Locate every blood parasite and identify its species.
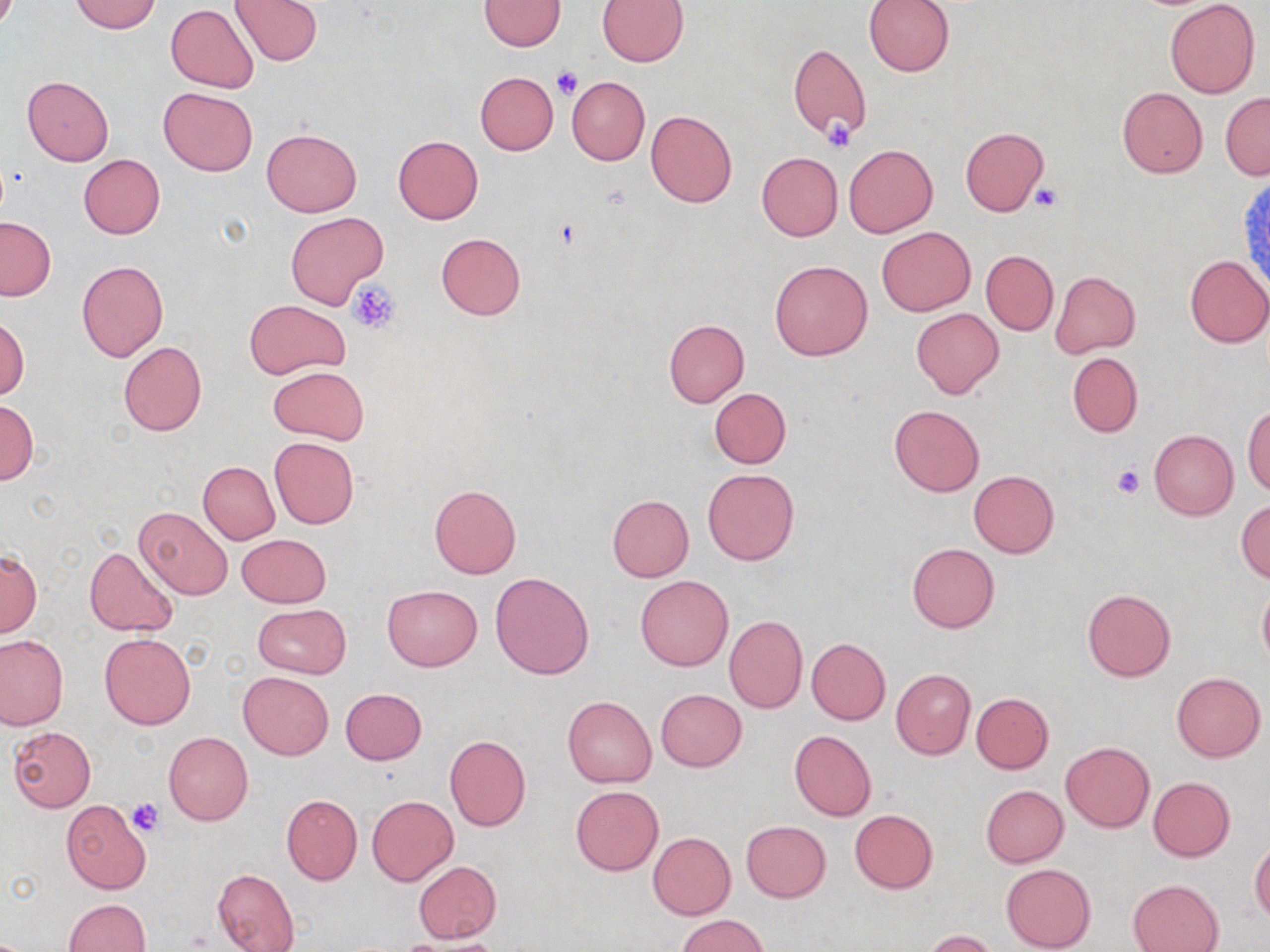

No blood parasites observed.

Summary:
  - Coordinate format: approximate bounding boxes as (x1, y1, x2, y2) in pixels
  - Uninfected red blood cell locations: (69, 0, 160, 33), (230, 0, 323, 66), (864, 0, 954, 76), (1165, 0, 1259, 99), (479, 1, 564, 51), (596, 1, 689, 65), (166, 5, 259, 93), (788, 45, 870, 142), (474, 71, 558, 154), (22, 76, 113, 166), (566, 77, 649, 165), (1117, 86, 1208, 178), (159, 87, 257, 175), (1220, 92, 1270, 179), (645, 110, 737, 209), (959, 126, 1048, 216), (262, 128, 362, 216), (393, 135, 483, 224), (844, 144, 937, 237), (756, 151, 843, 241), (79, 154, 165, 239), (285, 212, 388, 308), (0, 216, 55, 301), (877, 226, 975, 315), (435, 232, 526, 320), (981, 250, 1058, 334), (1184, 254, 1269, 347), (77, 260, 168, 361), (769, 260, 873, 361), (982, 261, 1137, 344), (1051, 272, 1140, 356), (243, 299, 348, 379), (911, 308, 1003, 399), (0, 317, 28, 401), (663, 319, 749, 408), (118, 341, 207, 436), (1067, 353, 1142, 437), (266, 366, 369, 445), (710, 388, 791, 468), (1, 399, 37, 485), (889, 404, 985, 497), (1244, 406, 1270, 497), (1149, 431, 1238, 519), (268, 437, 359, 528), (198, 462, 280, 545), (702, 469, 799, 565), (969, 470, 1059, 558), (429, 485, 522, 579), (607, 495, 694, 581), (1235, 500, 1270, 582), (135, 506, 233, 599), (236, 533, 331, 607), (907, 543, 999, 632), (85, 544, 180, 637), (0, 551, 40, 636), (491, 571, 595, 680), (635, 575, 734, 671), (1257, 580, 1270, 668), (382, 586, 483, 671), (1082, 589, 1175, 681), (253, 604, 351, 678), (724, 616, 807, 714), (100, 633, 195, 730), (0, 635, 68, 730), (806, 637, 890, 724), (891, 669, 975, 759), (238, 672, 333, 759), (1171, 672, 1265, 761), (340, 688, 427, 764), (656, 689, 746, 771), (972, 693, 1053, 773), (563, 695, 656, 787), (7, 725, 95, 813), (789, 730, 876, 821), (164, 731, 252, 825), (445, 734, 531, 831), (1060, 742, 1154, 833), (1148, 777, 1235, 862), (571, 785, 663, 876), (980, 785, 1068, 868), (281, 794, 362, 885), (367, 796, 458, 884), (61, 799, 152, 894), (849, 809, 938, 894), (741, 820, 831, 902), (648, 832, 736, 920), (1250, 840, 1270, 924), (413, 861, 501, 942), (1001, 863, 1095, 951), (213, 868, 299, 952), (1129, 879, 1224, 952), (63, 898, 150, 951), (676, 914, 770, 952), (922, 929, 997, 952), (401, 935, 507, 952)
  - Platelet locations: (551, 67, 583, 99), (822, 120, 855, 153), (1032, 184, 1063, 211), (349, 281, 401, 333), (1112, 463, 1146, 498), (128, 800, 163, 838)
  - Slide-level diagnosis: no evidence of blood parasites
  - Preparation: thin blood film
  - Field of view: one of a larger specimen
  - Magnification: 1000x
  - Modality: light microscopy
  - Stain: May-Grünwald-Giemsa
  - Image size: 1270×952 pixels